Identify the cell.
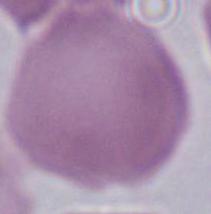

This is an erythrocyte.

modality: micrograph
magnification: 1000x